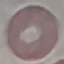

malaria status = uninfected
preparation = thin smear
capture = smartphone camera at the microscope eyepiece
image type = cell patch, automatically extracted from a larger field of view and resized to 64 × 64 pixels
stain = Giemsa